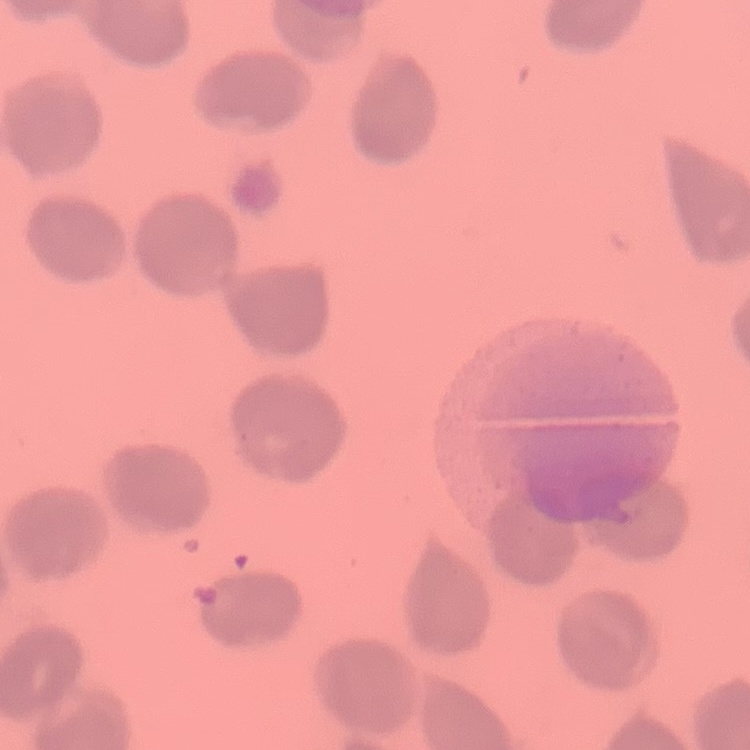 The red blood cells show no rouleaux formation. Field's or Giemsa stain. Thin blood film. One tile cut from a larger photomicrograph.